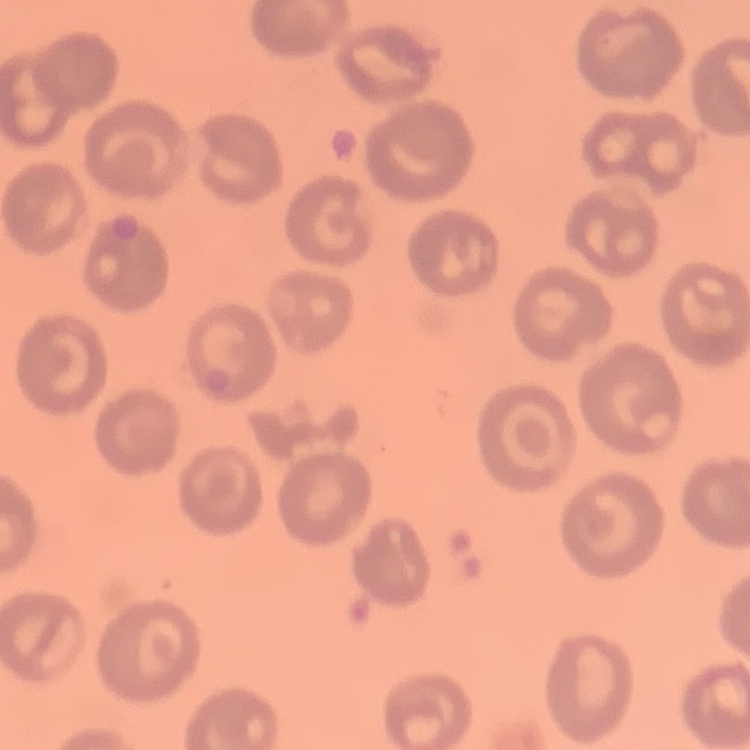

{
  "red_blood_cell_morphology": "no rouleaux formation",
  "preparation": "thin peripheral smear",
  "image_type": "one tile cut from a larger photomicrograph",
  "stain": "Field's or Giemsa"
}